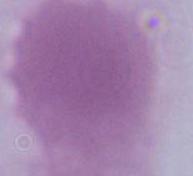
modality: micrograph
identification: red blood cell
magnification: 1000x